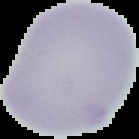

Summary:
  - Image type: cell region segmented out of the field of view; surrounding area masked to black
  - Preparation: thin blood film
  - Image size: 139×139 pixels
  - Result: no Plasmodium parasites detected